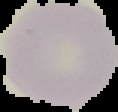
image_type: cell region segmented out of the field of view; surrounding area masked to black
image_size: 118×112 pixels
preparation: thin blood smear
result: no Plasmodium parasites detected